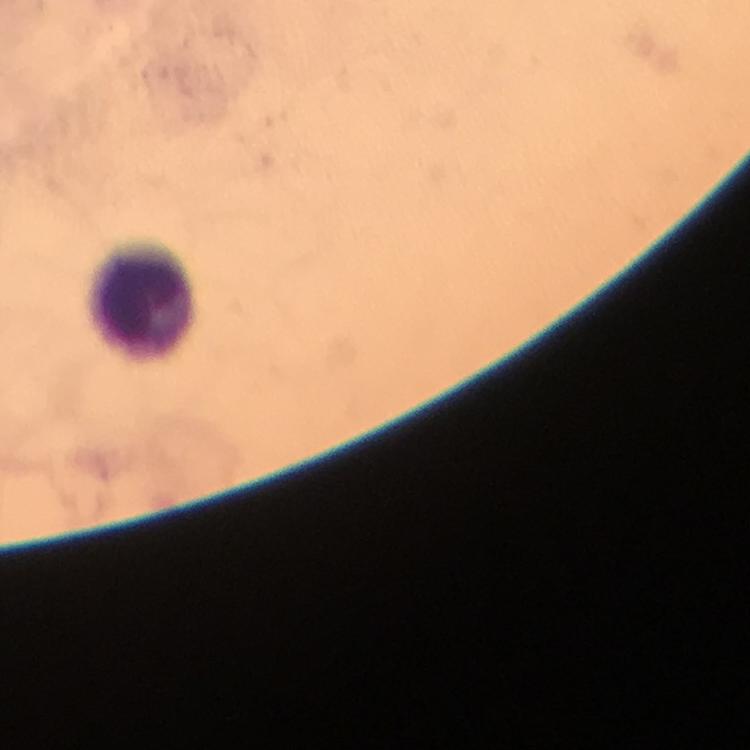
Approximate centers as (x, y) in pixels. Leukocyte locations: (144, 305). Thick blood smear. Plasmodium parasites: none seen. From a diagnostic examination for malaria. 100x magnification. Smartphone photograph taken through a microscope. Giemsa-stained preparation. Image is 750×750 pixels. Cropped region of a single field of view. Immersion oil applied.